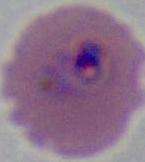
magnification = 400x or 1000x
modality = photomicrograph
identification = Plasmodium